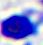
{
  "magnification": "400x",
  "identification": "leukocyte",
  "modality": "micrograph"
}